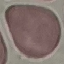
{
  "result": "negative for malaria parasites",
  "preparation": "thin smear",
  "stain": "Giemsa",
  "image_type": "cell patch, automatically extracted from a larger field of view and resized to 64 × 64 pixels",
  "capture": "smartphone camera at the microscope eyepiece"
}